Assess this cell for malaria.
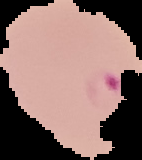
Parasitized.

Image is 142×160 pixels. Cell region segmented out of the field of view; the surrounding area is masked to black. From a thin blood smear.